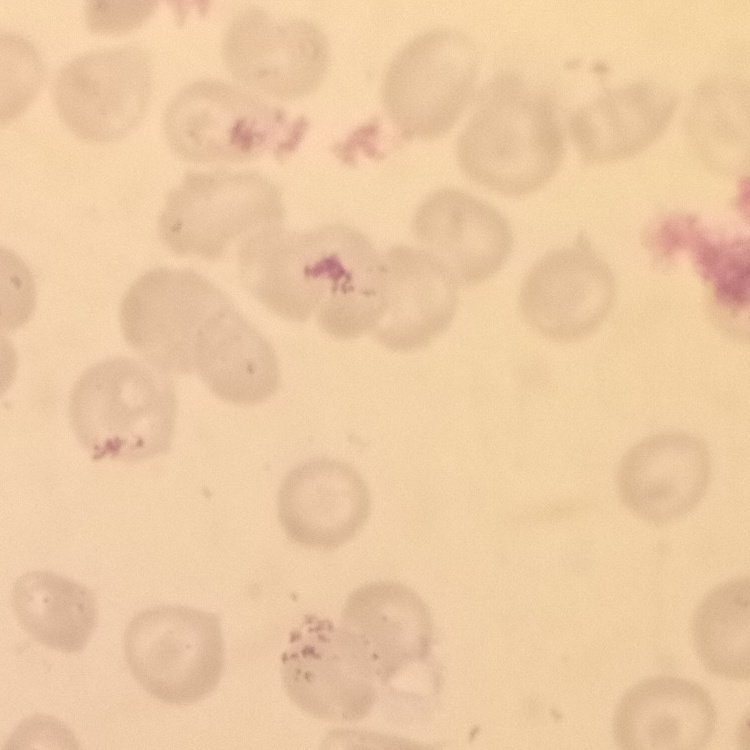

Summary:
  - Erythrocyte morphology: no rouleaux formation
  - Image type: square crop of a larger photomicrograph
  - Stain: Field's or Giemsa
  - Preparation: thin blood smear